Name the blood parasite species.
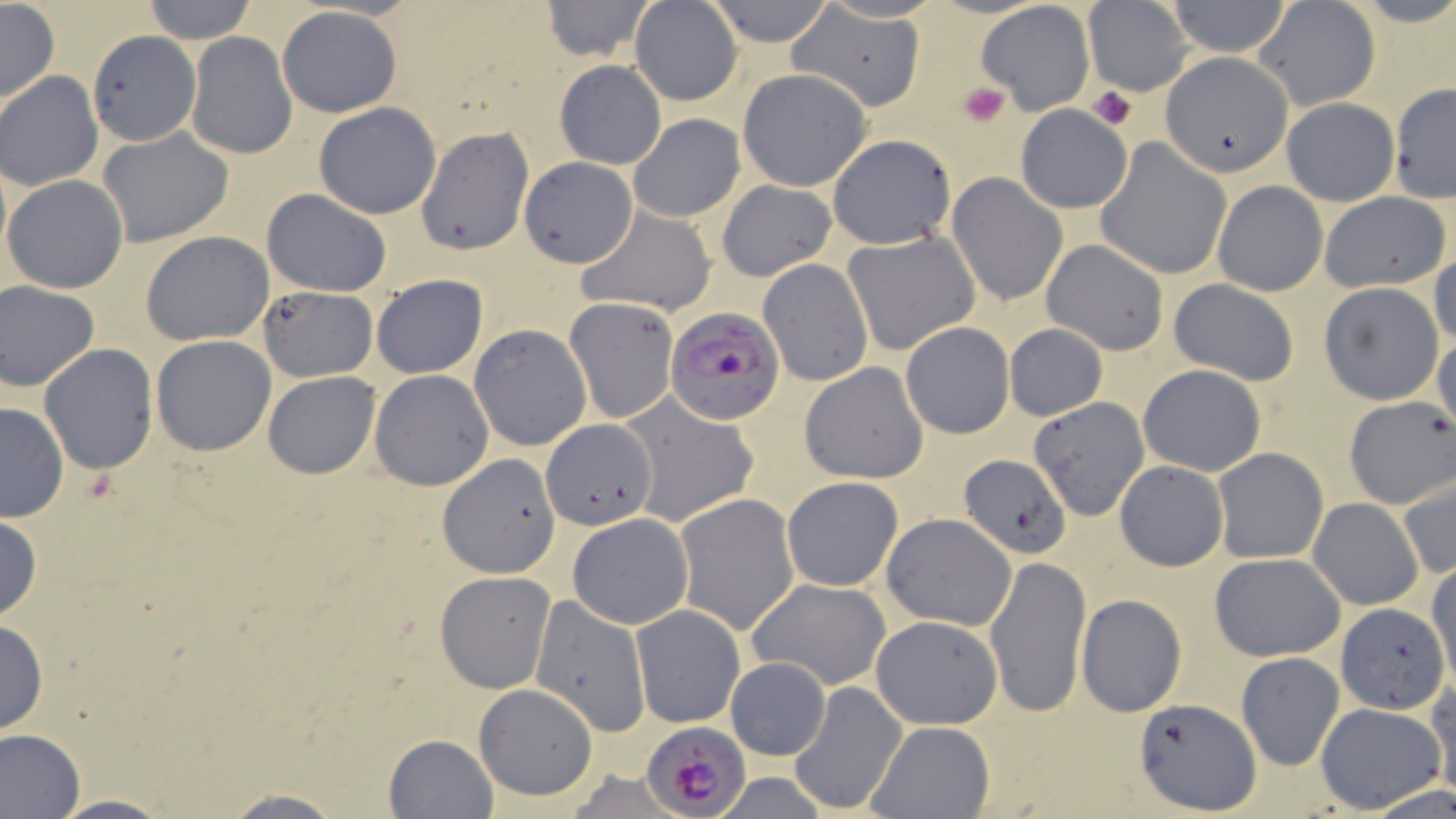
Plasmodium falciparum.

Approximate bounding boxes as [x1, y1, x2, y2] in pixels. Platelet locations: [958, 81, 1008, 127], [1088, 85, 1138, 132]. Uninfected red blood cell locations: [140, 0, 258, 44], [703, 0, 837, 47], [1163, 0, 1295, 57], [1251, 0, 1381, 111], [540, 1, 658, 63], [629, 1, 743, 106], [977, 1, 1096, 116], [1084, 1, 1196, 95], [0, 3, 59, 104], [790, 4, 927, 111], [278, 7, 403, 118], [88, 30, 200, 144], [185, 32, 296, 160], [1157, 51, 1294, 176], [554, 61, 666, 169], [737, 69, 872, 192], [0, 71, 103, 191], [1388, 84, 1456, 203], [1281, 99, 1399, 206], [313, 101, 441, 218], [1015, 104, 1131, 213], [628, 112, 745, 222], [1054, 121, 1180, 259], [414, 125, 534, 256], [97, 127, 234, 247], [828, 133, 957, 248], [1094, 138, 1232, 280], [519, 158, 637, 268], [946, 173, 1068, 305], [2, 174, 130, 294], [717, 179, 837, 281], [1211, 180, 1328, 297], [261, 188, 392, 297], [1319, 191, 1451, 292], [575, 206, 718, 316], [844, 230, 980, 356], [140, 231, 275, 345], [1042, 239, 1169, 355], [1430, 250, 1456, 349], [758, 258, 873, 387], [371, 273, 488, 379], [1166, 277, 1301, 386], [0, 282, 100, 391], [1317, 282, 1445, 405], [258, 286, 377, 380], [563, 297, 679, 425], [900, 320, 1015, 439], [1003, 323, 1109, 422], [469, 324, 591, 451], [1431, 332, 1456, 428], [151, 335, 277, 455], [39, 344, 159, 475], [799, 362, 927, 485], [1137, 363, 1268, 477], [369, 369, 493, 490], [262, 371, 381, 478], [618, 392, 760, 530], [1028, 395, 1150, 522], [1342, 395, 1456, 510], [0, 402, 70, 522], [542, 420, 657, 531], [1210, 447, 1330, 564], [438, 453, 561, 577], [957, 454, 1071, 559], [1116, 460, 1228, 571], [1397, 472, 1455, 581], [780, 475, 904, 592], [673, 492, 799, 636], [1308, 498, 1425, 609], [883, 512, 1016, 632], [566, 513, 693, 627], [0, 515, 44, 623], [984, 552, 1091, 721], [1208, 552, 1346, 662], [1427, 562, 1456, 691], [434, 571, 557, 693], [747, 578, 892, 689], [1077, 593, 1188, 717], [531, 595, 651, 738], [633, 603, 744, 726], [1336, 603, 1447, 714], [869, 615, 1003, 729], [0, 616, 48, 736], [814, 627, 942, 786], [1235, 651, 1345, 771], [724, 656, 832, 760], [1427, 680, 1456, 794], [790, 681, 906, 816], [473, 683, 599, 800], [1133, 699, 1261, 813], [1314, 702, 1447, 814], [866, 720, 995, 817], [0, 727, 86, 819], [382, 734, 498, 819], [215, 791, 354, 819], [49, 794, 172, 817]. Plasmodium falciparum-infected red blood cell locations: [665, 306, 783, 424], [645, 719, 751, 816]. 1000x magnification. One field of a larger specimen. Image is 1456×819 pixels. Thin blood smear. Light microscopy. May-Grünwald-Giemsa stain.